Classify this cell by malaria status.
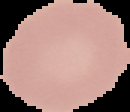

Uninfected.

Summary:
  - Image size: 130×112 pixels
  - Preparation: thin blood smear
  - Image type: segmented cell region with the area outside set to black